Name the blood parasite species.
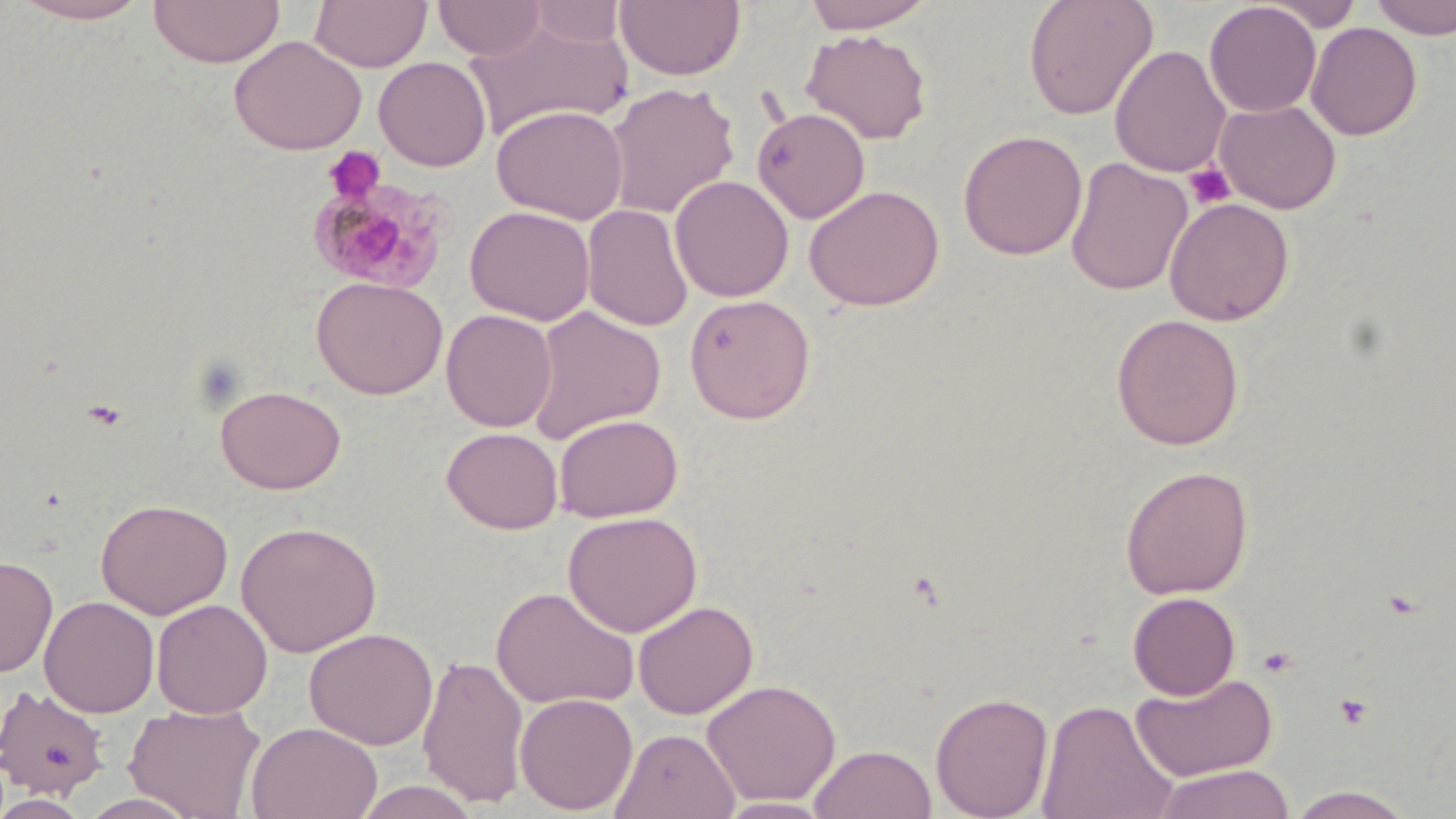
Plasmodium malariae.

{
  "image_size": "1456×819 pixels",
  "preparation": "thin blood smear",
  "platelet_locations": "approximate bounding boxes as [x1, y1, x2, y2] in pixels: [323, 147, 387, 204], [1184, 163, 1235, 210], [1258, 645, 1298, 677], [1335, 693, 1373, 729]",
  "magnification": "1000x",
  "uninfected_red_blood_cell_locations": "approximate bounding boxes as [x1, y1, x2, y2] in pixels: [7, 0, 152, 24], [148, 0, 285, 68], [309, 0, 432, 73], [434, 0, 546, 60], [616, 0, 746, 82], [800, 0, 937, 33], [1022, 0, 1159, 120], [1369, 0, 1456, 39], [1204, 1, 1321, 117], [1262, 1, 1365, 31], [526, 2, 628, 48], [465, 17, 633, 141], [1306, 21, 1422, 140], [801, 28, 933, 145], [229, 35, 367, 155], [1110, 45, 1231, 178], [373, 57, 491, 172], [604, 83, 740, 219], [1215, 99, 1341, 213], [491, 103, 629, 225], [752, 106, 870, 224], [958, 129, 1087, 259], [1065, 156, 1192, 297], [669, 175, 794, 302], [804, 185, 944, 311], [1164, 197, 1294, 326], [582, 203, 693, 332], [465, 205, 595, 325], [311, 276, 448, 399], [683, 294, 816, 424], [526, 305, 666, 444], [441, 309, 557, 432], [1110, 313, 1245, 450], [215, 384, 346, 494], [554, 413, 684, 522], [442, 427, 563, 534], [1119, 465, 1254, 600], [95, 498, 233, 619], [562, 511, 702, 637], [236, 520, 382, 657], [0, 554, 58, 677], [491, 585, 639, 710], [1127, 591, 1241, 700], [39, 595, 159, 718], [151, 599, 273, 718], [633, 600, 759, 719], [304, 627, 438, 749], [418, 653, 529, 809], [1130, 671, 1279, 782], [702, 678, 841, 806], [1, 683, 110, 799], [930, 691, 1054, 819], [515, 692, 638, 814], [1036, 698, 1178, 819], [124, 702, 266, 818], [246, 721, 382, 819], [612, 727, 740, 819], [809, 744, 937, 819], [1150, 763, 1295, 819], [352, 779, 484, 819], [1285, 785, 1419, 818], [77, 792, 202, 818], [0, 793, 92, 818], [714, 796, 836, 818]",
  "field_of_view": "single",
  "plasmodium_malariae_infected_red_blood_cell_locations": "approximate bounding boxes as [x1, y1, x2, y2] in pixels: [306, 174, 452, 294]",
  "modality": "light microscopy",
  "stain": "May-Grünwald-Giemsa"
}